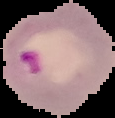

image size = 115×118 pixels
preparation = thin blood film
malaria status = parasitized
image type = segmented cell region on a black background